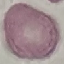

malaria_status: uninfected
capture: smartphone camera at the microscope eyepiece
stain: Giemsa
image_type: cell patch, automatically extracted from a larger field of view and resized to 64 × 64 pixels
preparation: thin blood film